Locate the cells, classifying each as a parasitized RBC, an uninfected RBC, or a WBC.
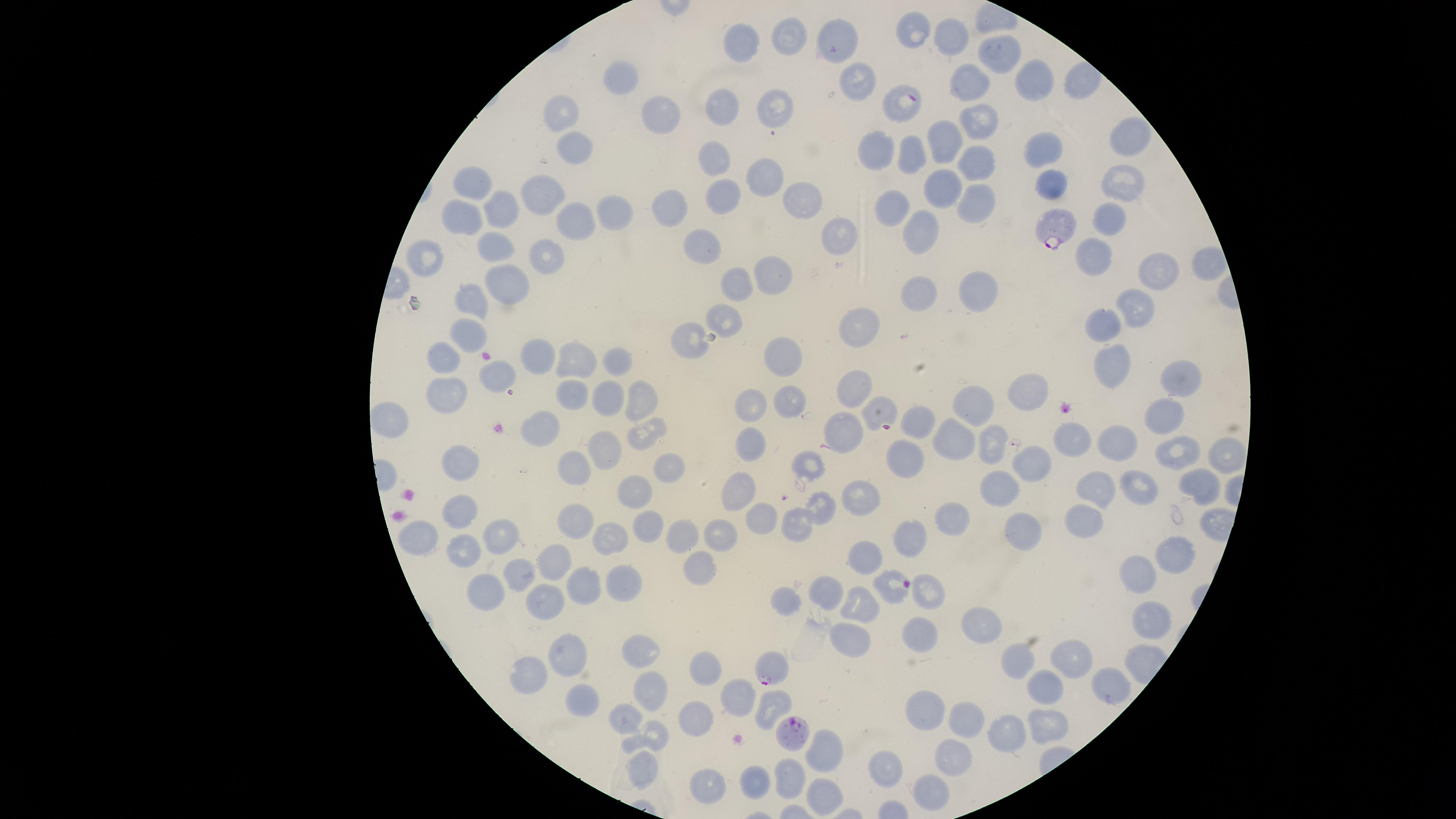

Approximate marker points as [x, y] in pixels.
Parasitized RBCs: [906, 100], [1056, 225], [769, 666], [798, 733].
Uninfected RBCs: [913, 30], [790, 35], [949, 38], [837, 39], [746, 41], [996, 53], [622, 79], [1033, 81], [971, 83], [861, 84], [774, 107], [723, 110], [563, 113], [663, 113], [979, 121], [943, 134], [1128, 135], [1043, 148], [571, 150], [875, 150], [907, 155], [714, 159], [976, 159], [763, 178], [473, 181], [1053, 182], [1125, 187], [942, 190], [543, 194], [720, 194], [801, 198], [971, 200], [896, 204], [504, 210], [611, 210], [665, 210], [466, 221], [575, 221], [1104, 222], [924, 229], [841, 230], [502, 244], [705, 246], [1095, 256], [546, 258], [426, 261], [1161, 267], [767, 276], [507, 279], [736, 282], [921, 290], [979, 290], [468, 301], [1138, 309], [725, 316], [1106, 319], [860, 326], [470, 336], [692, 336], [445, 355], [536, 355], [1110, 356], [622, 358], [570, 359], [782, 360], [499, 373], [1173, 379], [859, 386], [1033, 392], [645, 395], [571, 397], [446, 398], [607, 399], [752, 402], [790, 403], [976, 405], [882, 410], [391, 419], [918, 419], [1160, 419], [543, 427], [843, 427], [646, 431], [994, 437], [1077, 439], [952, 441], [1121, 444], [755, 446], [1175, 450], [606, 452], [903, 455], [1220, 456], [1037, 460], [461, 463], [668, 464], [810, 466], [579, 469], [1196, 482], [1139, 486], [1000, 488], [1098, 488], [632, 489], [738, 491], [863, 495], [819, 508], [458, 513], [1081, 517], [950, 518], [584, 519], [765, 520], [642, 521], [798, 524], [1024, 528], [502, 533], [720, 535], [912, 535], [614, 536], [681, 538], [415, 542], [473, 553], [862, 554], [1172, 556], [556, 558], [698, 566], [517, 571], [1139, 576], [619, 578], [886, 583], [927, 585], [584, 587], [492, 592], [827, 593], [785, 598], [544, 601], [862, 602], [985, 621], [1151, 622], [852, 637], [925, 639], [566, 652], [646, 654], [1077, 656], [1017, 662], [704, 671], [529, 672], [1049, 683], [1112, 683], [651, 690], [731, 698], [775, 701], [581, 704], [627, 715], [924, 715], [697, 720], [972, 724], [1045, 731], [1008, 732], [652, 733], [825, 749], [956, 760], [644, 766], [885, 771], [752, 781], [792, 782], [707, 784], [931, 793], [823, 794].
No WBCs identified.

Summary:
  - Stain: Giemsa
  - Capture: smartphone photograph through the microscope eyepiece
  - Image size: 1456×819 pixels
  - Preparation: thin blood smear
  - Species: Plasmodium falciparum
  - Visible region: circular
  - Field of view: single